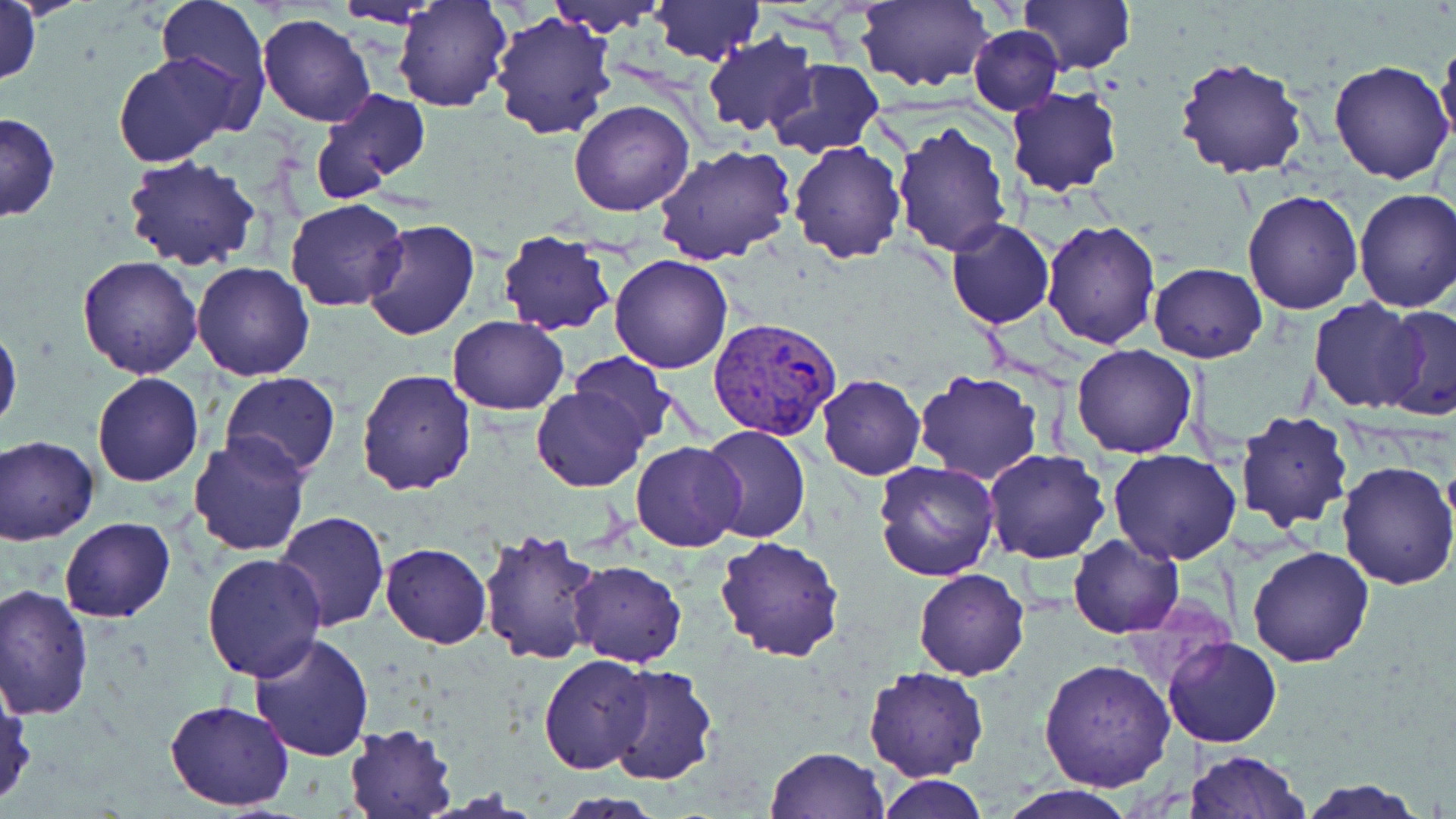

slide-level diagnosis = Plasmodium vivax
stain = May-Grünwald-Giemsa
Plasmodium vivax-infected red blood cell locations = approximate bounding boxes as (x1, y1, x2, y2) in pixels: (708, 317, 842, 440)
magnification = 1000x
uninfected red blood cell locations = approximate bounding boxes as (x1, y1, x2, y2) in pixels: (155, 0, 271, 111), (394, 0, 511, 111), (545, 0, 666, 32), (650, 0, 762, 65), (856, 0, 994, 93), (1018, 0, 1135, 75), (332, 2, 450, 27), (1, 3, 41, 92), (489, 9, 619, 141), (258, 12, 377, 128), (968, 25, 1063, 115), (701, 34, 817, 137), (1435, 36, 1456, 154), (113, 52, 241, 168), (1175, 57, 1308, 178), (768, 58, 883, 158), (1329, 61, 1455, 186), (311, 86, 430, 200), (1005, 87, 1124, 197), (569, 100, 694, 218), (1, 112, 60, 222), (892, 119, 1014, 256), (788, 140, 906, 263), (655, 144, 797, 266), (120, 155, 263, 274), (1352, 188, 1456, 312), (1241, 190, 1365, 314), (285, 199, 410, 313), (361, 219, 480, 341), (946, 219, 1054, 329), (1041, 220, 1161, 352), (497, 230, 617, 335), (611, 254, 732, 373), (77, 255, 202, 377), (191, 261, 316, 382), (1148, 263, 1267, 362), (1309, 298, 1428, 415), (1378, 305, 1456, 422), (447, 316, 569, 415), (0, 324, 22, 435), (1071, 344, 1199, 459), (571, 352, 675, 447), (355, 368, 476, 497), (911, 370, 1043, 486), (91, 372, 204, 487), (221, 372, 342, 477), (816, 374, 925, 479), (533, 389, 646, 491), (1234, 410, 1355, 532), (700, 425, 811, 545), (2, 434, 99, 544), (187, 436, 312, 558), (630, 441, 746, 552), (1109, 448, 1243, 566), (984, 449, 1110, 563), (1335, 460, 1456, 590), (873, 461, 1000, 583), (275, 511, 390, 632), (59, 517, 176, 623), (476, 528, 604, 668), (1067, 534, 1183, 639), (715, 535, 844, 661), (381, 543, 491, 648), (1246, 545, 1375, 666), (202, 553, 328, 684), (569, 560, 687, 667), (913, 567, 1029, 680), (1, 584, 95, 720), (249, 631, 377, 759), (1162, 636, 1283, 748), (538, 654, 654, 774), (1039, 658, 1174, 793), (604, 666, 718, 787), (863, 667, 986, 782), (0, 682, 35, 808), (164, 698, 294, 811), (342, 724, 458, 818), (768, 747, 888, 818), (1184, 750, 1309, 819), (876, 776, 989, 818), (1295, 778, 1431, 819), (999, 786, 1136, 819)
modality = optical microscopy
image size = 1456×819 pixels
field of view = single
preparation = thin blood smear